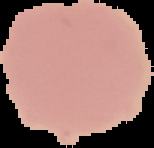
{
  "preparation": "thin blood film",
  "result": "no malaria parasites seen",
  "image_size": "154×148 pixels",
  "image_type": "cell region segmented out of the field of view; surrounding area masked to black"
}